Report the malaria status of this cell.
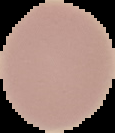

Uninfected.

Cell region segmented out of the field of view; the surrounding area is masked to black. Image is 115×133 pixels. From a thin blood film.